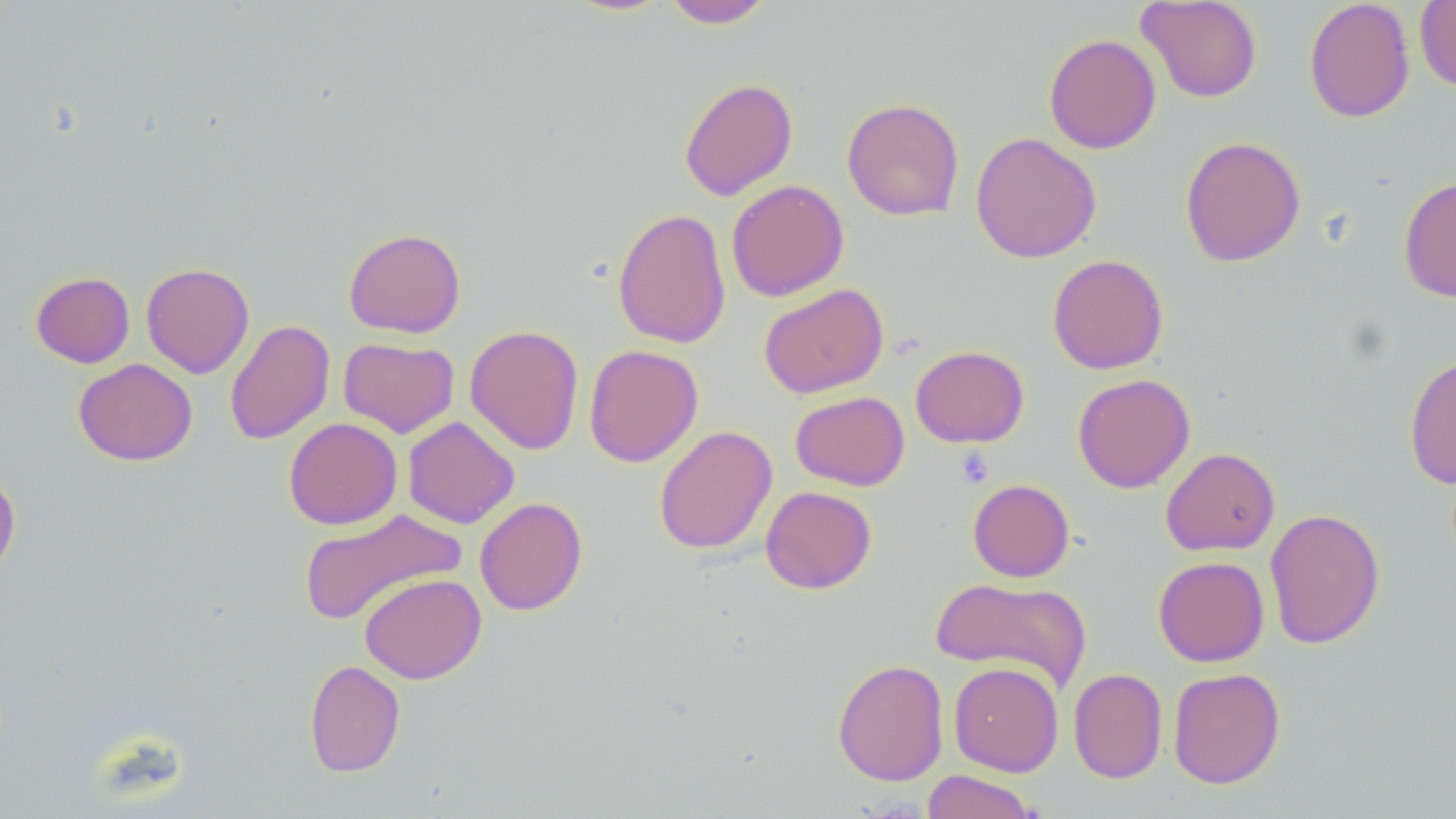

slide-level diagnosis = no evidence of blood parasites
field of view = single
platelet locations = approximate bounding boxes as (x1,y1)-(x2,y2) corner pairs in pixels: (956,447)-(994,487)
image size = 1456×819 pixels
magnification = 1000x
modality = optical microscopy
preparation = thin blood film
stain = May-Grünwald-Giemsa
uninfected red blood cell locations = approximate bounding boxes as (x1,y1)-(x2,y2) corner pairs in pixels: (563,0)-(673,16), (661,0)-(774,28), (1137,0)-(1262,103), (1304,0)-(1415,123), (1414,1)-(1456,92), (1043,33)-(1161,153), (678,77)-(798,201), (841,98)-(965,221), (970,132)-(1102,263), (1180,135)-(1306,268), (1398,176)-(1456,302), (726,179)-(850,301), (612,208)-(731,349), (343,228)-(466,338), (1047,254)-(1169,375), (141,262)-(255,378), (30,271)-(135,368), (759,284)-(888,398), (224,320)-(335,445), (464,324)-(584,455), (338,337)-(459,438), (584,344)-(703,467), (910,345)-(1030,448), (1404,352)-(1456,490), (73,359)-(197,466), (1072,374)-(1195,493), (791,391)-(909,490), (402,416)-(520,528), (283,417)-(403,530), (653,425)-(778,554), (1160,446)-(1280,555), (0,468)-(21,578), (968,479)-(1075,582), (760,486)-(877,594), (474,497)-(588,616), (297,508)-(467,627), (1264,508)-(1385,649), (1153,556)-(1269,666), (359,572)-(486,684), (930,576)-(1092,692), (304,659)-(406,778), (832,659)-(949,786), (948,661)-(1064,776), (1068,667)-(1167,783), (1168,667)-(1286,789), (922,770)-(1040,819)